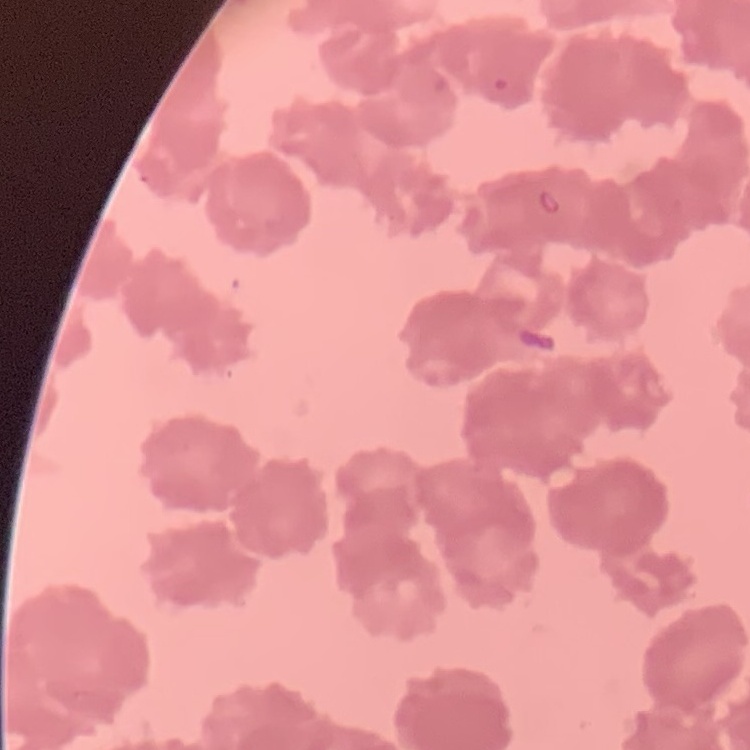

Summary:
  - Red blood cell morphology: rouleaux formation
  - Stain: Field's or Giemsa
  - Image type: square crop of a larger photomicrograph
  - Preparation: thin peripheral smear